Assess for malaria.
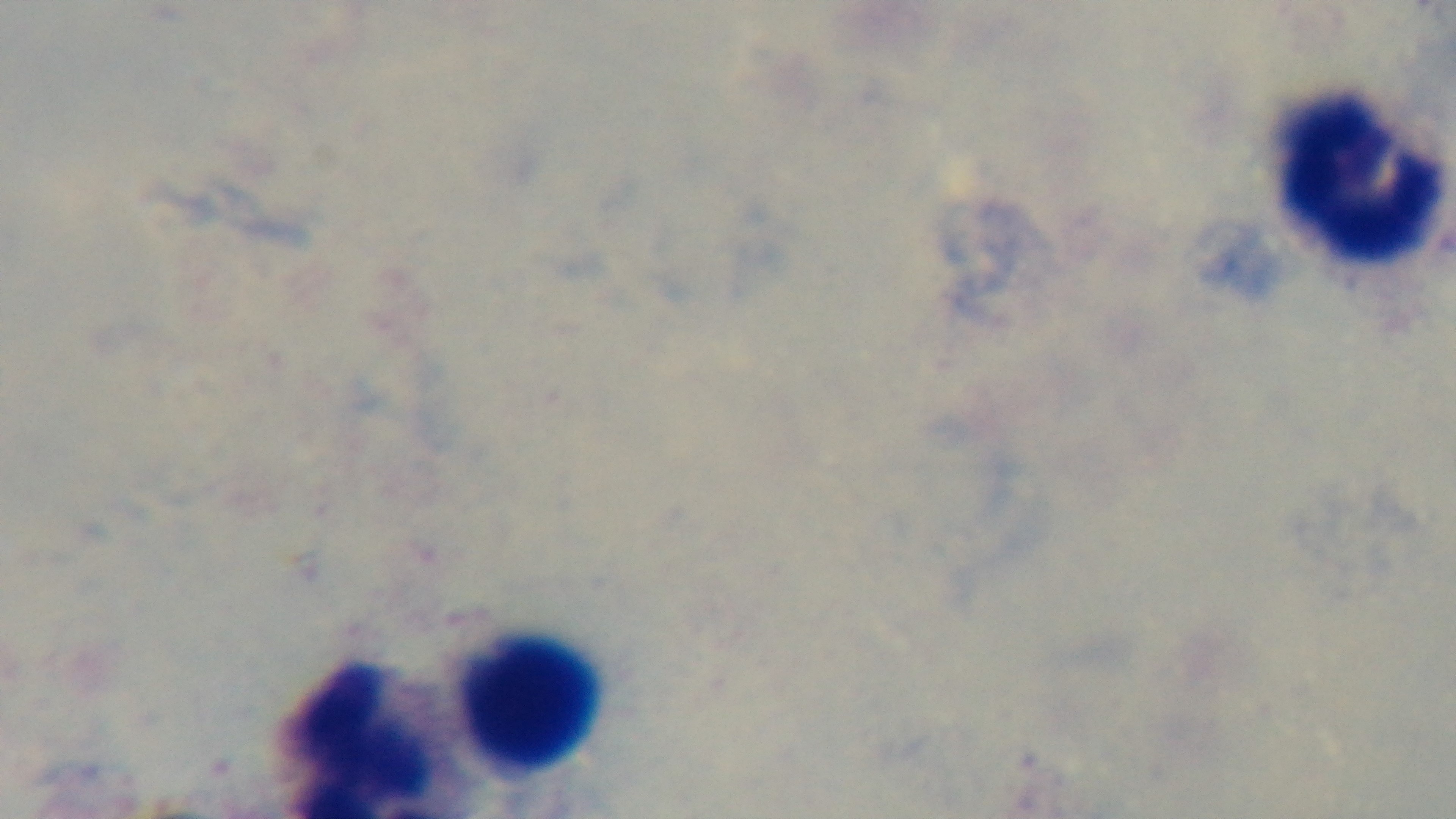
It is uninfected.

Summary:
  - Stain: Giemsa
  - Capture: mounted 4K digital camera
  - Preparation: thick smear
  - Field of view: single
  - Modality: light microscopy
  - Objective: 100x oil immersion